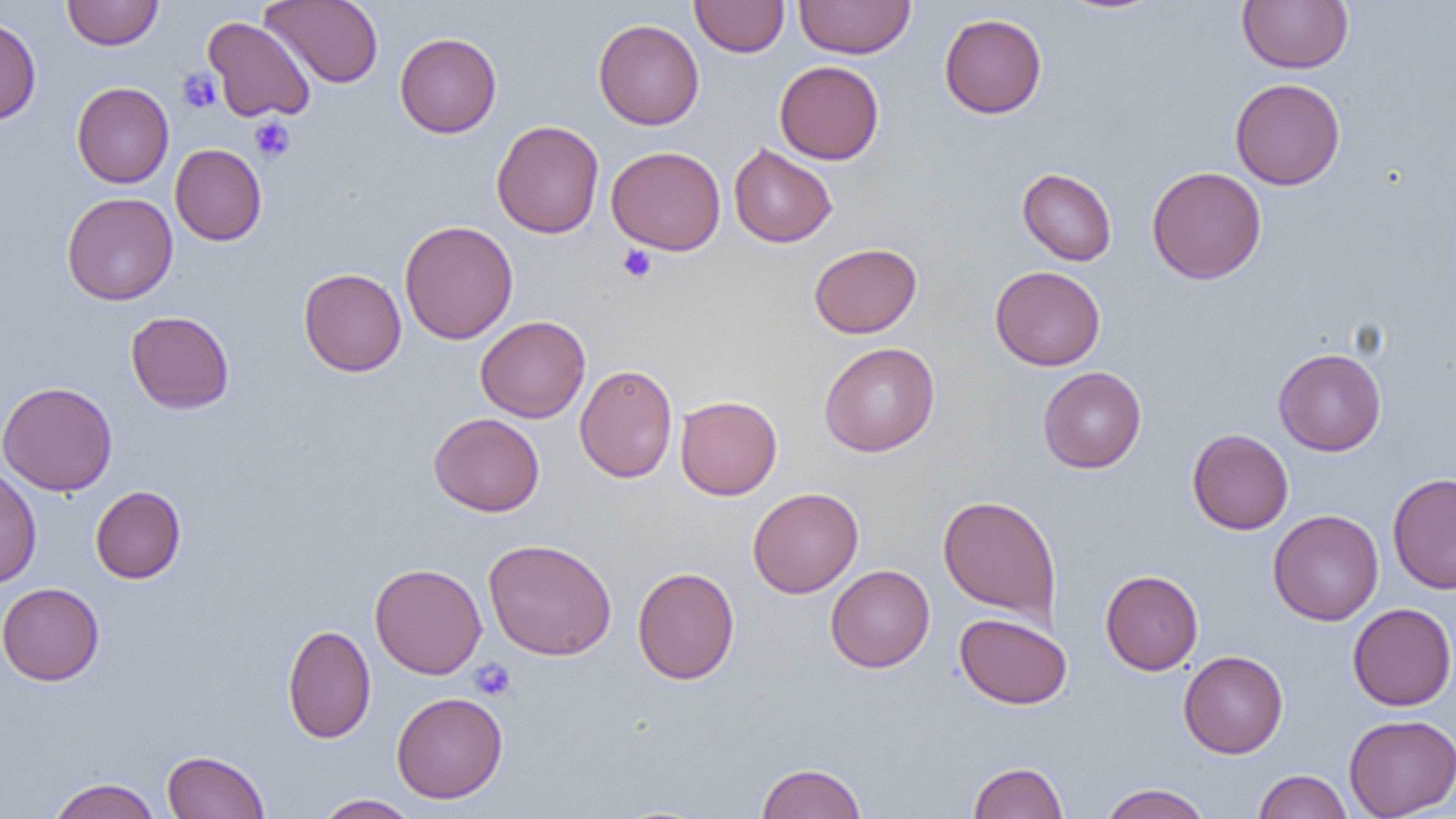

Summary:
  - Coordinate format: approximate bounding boxes as [x1, y1, x2, y2] in pixels
  - Uninfected red blood cell locations: [62, 0, 163, 49], [261, 0, 384, 88], [690, 0, 789, 57], [794, 0, 915, 58], [1056, 0, 1168, 16], [1237, 0, 1354, 74], [939, 14, 1047, 118], [0, 15, 41, 125], [203, 16, 316, 123], [593, 19, 704, 130], [394, 32, 501, 138], [774, 60, 885, 164], [1230, 78, 1346, 189], [71, 82, 174, 188], [491, 120, 604, 238], [728, 143, 838, 248], [170, 144, 266, 245], [606, 145, 726, 255], [1147, 166, 1266, 285], [1017, 167, 1117, 266], [61, 191, 178, 305], [399, 220, 518, 344], [809, 242, 922, 339], [990, 266, 1105, 371], [298, 268, 407, 376], [125, 310, 235, 413], [475, 315, 591, 422], [819, 342, 940, 457], [1274, 348, 1386, 456], [575, 364, 678, 483], [1037, 366, 1147, 473], [0, 381, 118, 496], [675, 395, 783, 500], [428, 413, 544, 517], [1187, 429, 1294, 534], [0, 466, 41, 588], [1387, 473, 1456, 594], [90, 485, 186, 583], [747, 487, 863, 598], [937, 494, 1062, 626], [1268, 509, 1384, 625], [482, 538, 617, 661], [370, 562, 486, 679], [825, 565, 935, 672], [632, 566, 740, 684], [1100, 569, 1203, 675], [0, 583, 104, 685], [1347, 602, 1456, 711], [954, 612, 1072, 709], [282, 624, 376, 744], [1178, 651, 1288, 758], [391, 692, 508, 803], [1343, 714, 1456, 819], [162, 750, 270, 819], [967, 761, 1069, 819], [755, 762, 867, 819], [1252, 769, 1353, 819], [48, 777, 162, 819], [1098, 783, 1213, 819], [314, 794, 421, 818]
  - Platelet locations: [177, 68, 222, 114], [248, 115, 295, 162], [618, 245, 657, 284], [469, 659, 516, 701]
  - Slide-level diagnosis: no evidence of blood parasites
  - Field of view: one of a larger specimen
  - Magnification: 1000x
  - Preparation: thin blood smear
  - Modality: optical microscopy
  - Image size: 1456×819 pixels